State the preparation type.
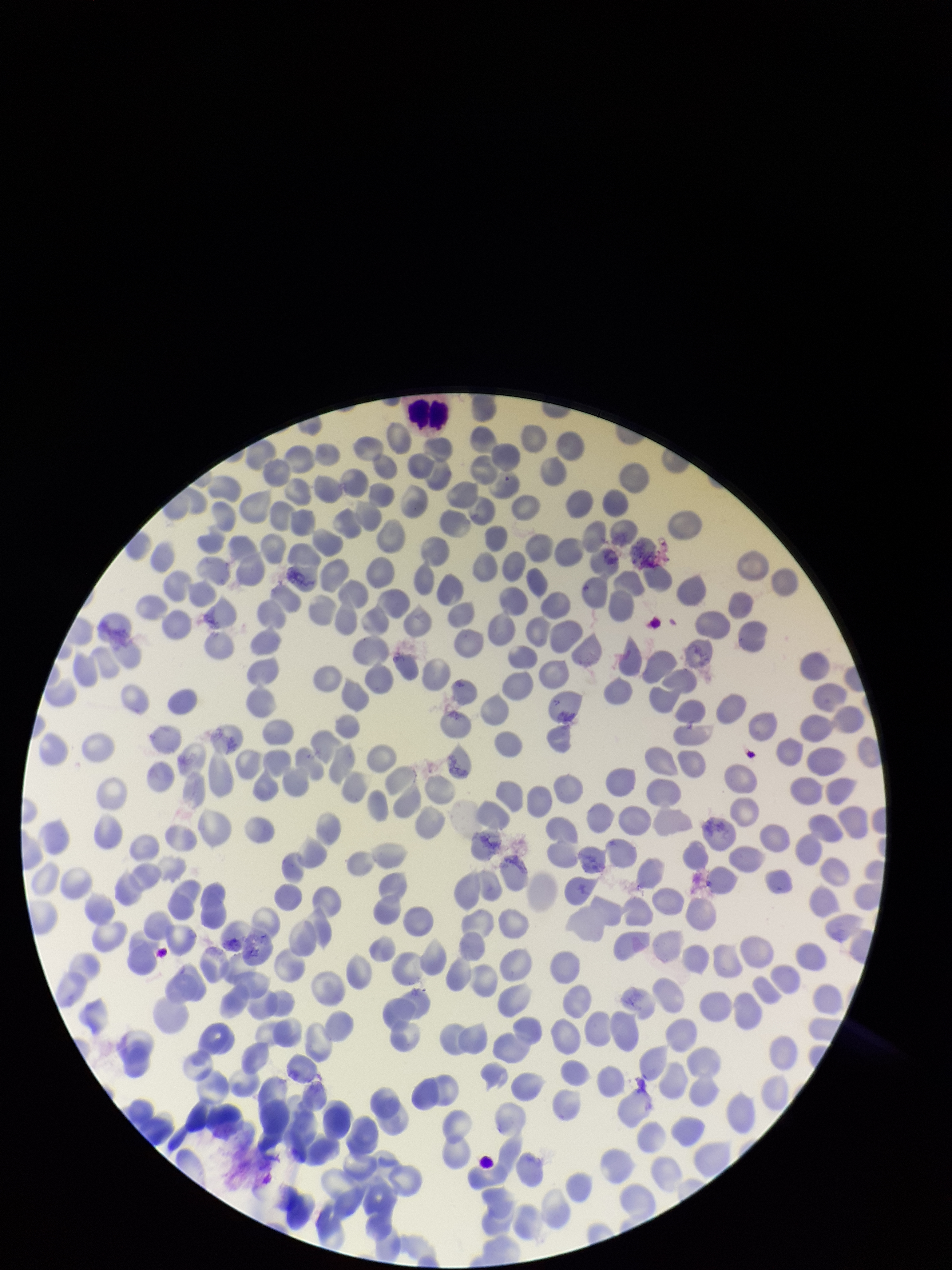
A thin smear.

Red blood cell count: 300. One field from this slide. Image is 952×1270 pixels. Parasitized red blood cell count: 0. Patient malaria status: negative. Stained with Giemsa. Parasitized red blood cells: none detected. Smartphone photograph taken through the eyepiece of a microscope.